Name the cell type shown.
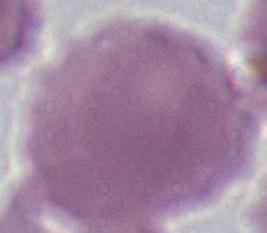

An erythrocyte.

{
  "modality": "photomicrograph",
  "magnification": "1000x"
}